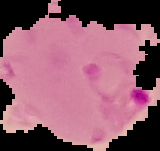
Image is 160×151 pixels. Malaria status: parasitized. Segmented cell region on a black background. From a thin blood film.